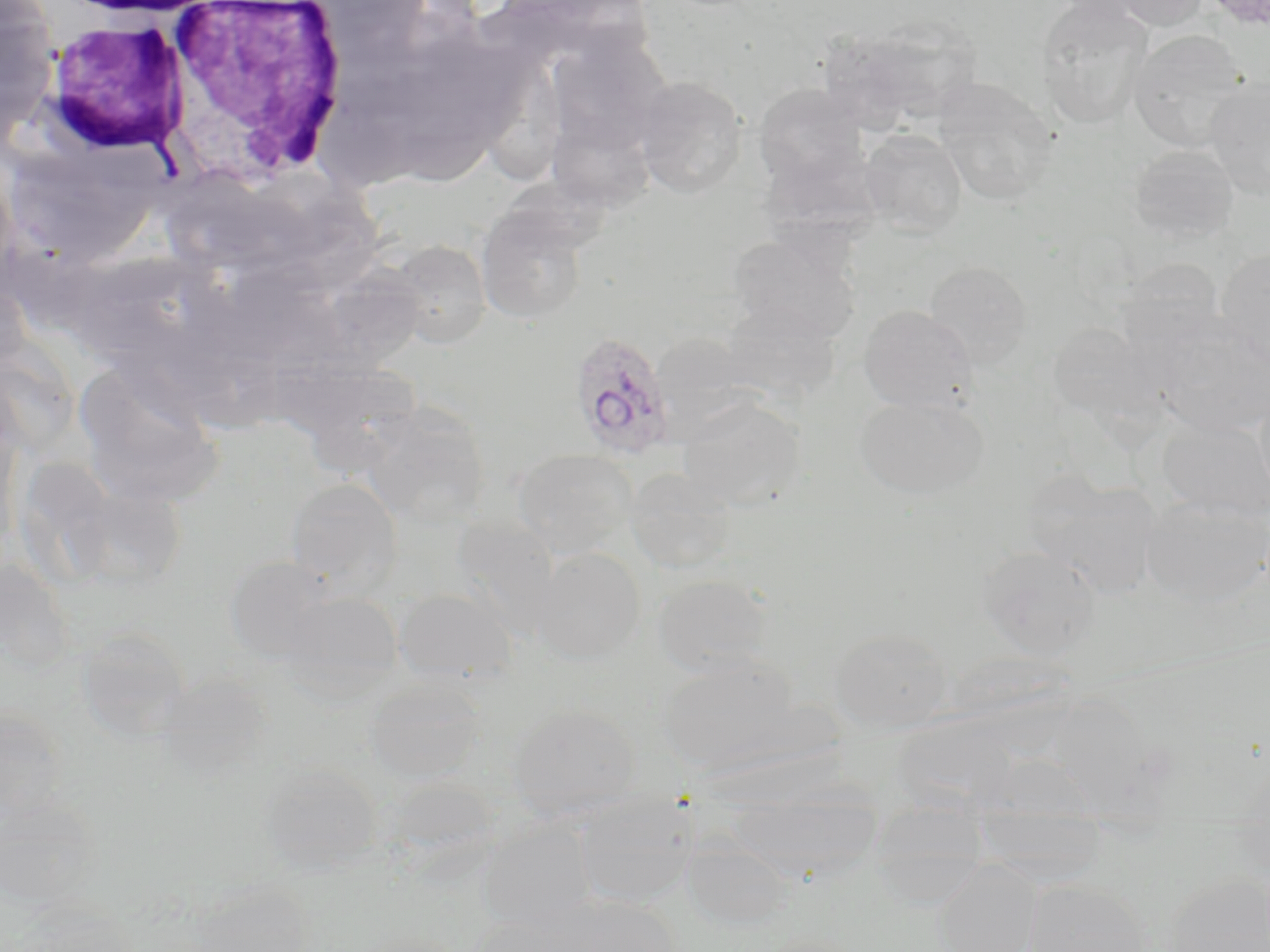

slide_level_diagnosis: Plasmodium ovale
magnification: 1000x
plasmodium_ovale_infected_red_blood_cell_locations: 'approximate bounding boxes as (x1,y1)-(x2,y2) corner pairs in pixels: (576,337)-(684,466)'
image_size: 1270×952 pixels
field_of_view: single
modality: optical microscopy
stain: May-Grünwald-Giemsa
uninfected_red_blood_cell_locations: 'approximate bounding boxes as (x1,y1)-(x2,y2) corner pairs in pixels: (1037,0)-(1154,130), (1104,0)-(1210,31), (0,3)-(58,137), (854,18)-(985,124), (1128,30)-(1250,152), (558,48)-(673,146), (487,57)-(567,181), (633,75)-(748,198), (933,77)-(1058,205), (1203,77)-(1270,201), (752,83)-(867,187), (549,124)-(663,224), (860,129)-(967,238), (760,143)-(885,245), (1128,144)-(1239,245), (475,200)-(591,325), (728,232)-(861,343), (389,240)-(492,349), (1216,246)-(1270,369), (73,252)-(220,370), (1116,258)-(1225,352), (924,261)-(1033,370), (329,263)-(435,388), (721,301)-(843,404), (858,306)-(977,412), (1151,315)-(1270,438), (1047,321)-(1161,427), (73,362)-(227,510), (1253,380)-(1270,506), (854,394)-(989,501), (677,395)-(806,510), (359,403)-(491,527), (1157,416)-(1270,521), (512,449)-(638,558), (25,458)-(110,580), (624,468)-(736,574), (285,477)-(403,598), (1035,479)-(1161,596), (1141,494)-(1270,605), (975,545)-(1100,658), (531,547)-(645,664), (224,556)-(337,661), (652,573)-(774,677), (393,588)-(517,686), (277,591)-(404,701), (77,628)-(191,738), (830,628)-(953,734), (658,656)-(803,777), (364,677)-(486,782), (508,704)-(642,821), (0,705)-(69,832), (892,715)-(1018,817), (261,762)-(382,874), (721,776)-(886,883), (573,791)-(698,909), (476,820)-(596,933), (681,837)-(794,931), (933,861)-(1041,952), (1160,873)-(1270,952), (1022,880)-(1152,952), (185,882)-(315,952), (542,894)-(682,952), (461,916)-(587,952)'
preparation: thin blood smear
white_blood_cell_locations: 'approximate bounding boxes as (x1,y1)-(x2,y2) corner pairs in pixels: (160,2)-(353,184), (37,19)-(189,162)'